Locate platelets.
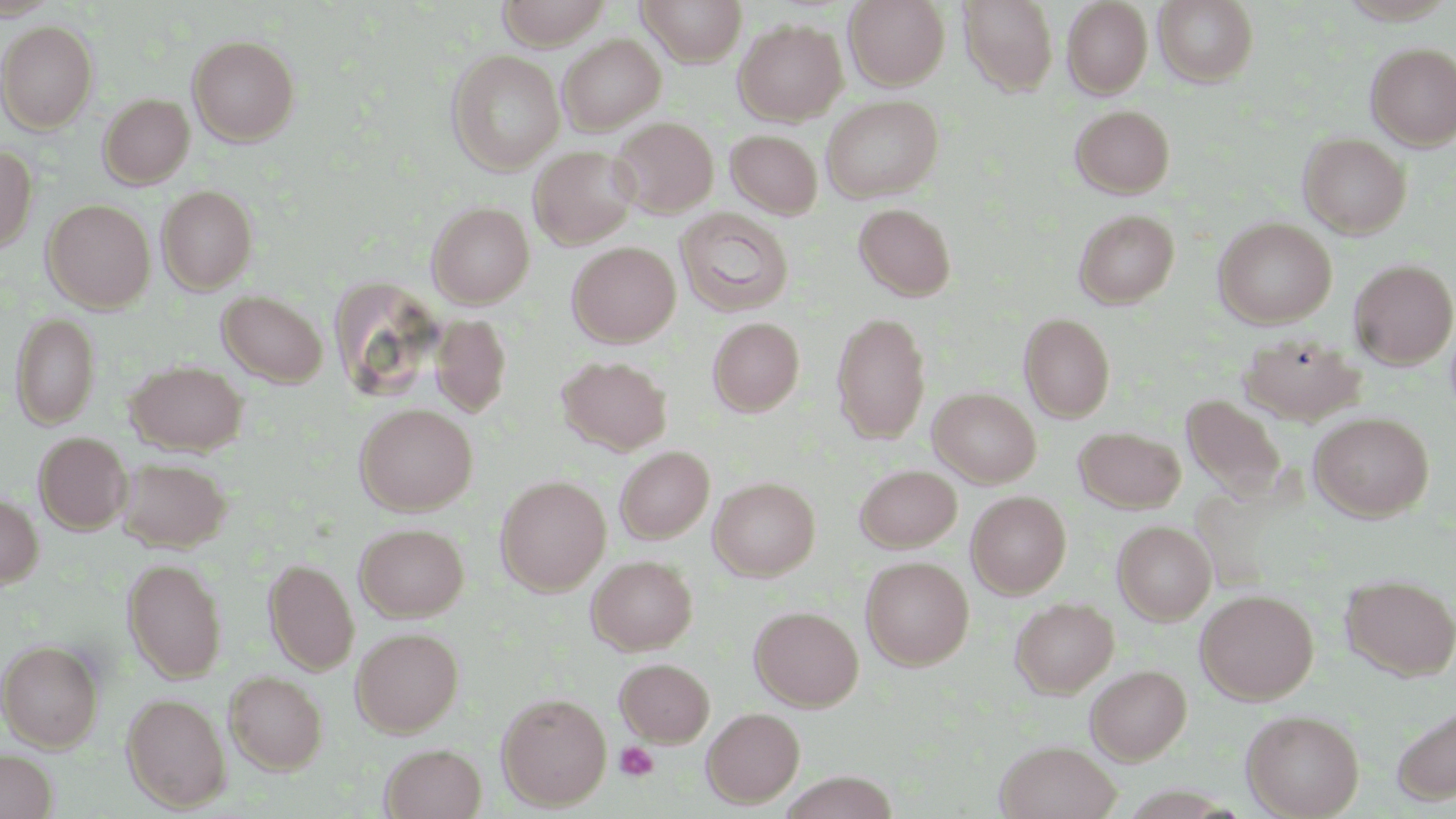

Approximate bounding boxes as (x1, y1, x2, y2) in pixels.
Platelets: (614, 740, 659, 782).

Uninfected red blood cell locations: (0, 0, 60, 19), (496, 0, 612, 48), (638, 0, 747, 66), (844, 0, 950, 89), (959, 0, 1059, 94), (1153, 0, 1258, 86), (1062, 1, 1153, 98), (733, 19, 847, 125), (0, 20, 99, 132), (188, 34, 300, 145), (558, 34, 665, 135), (1366, 42, 1456, 150), (446, 49, 565, 173), (99, 93, 194, 189), (822, 95, 943, 202), (1071, 105, 1175, 198), (610, 117, 719, 217), (726, 129, 822, 219), (1298, 132, 1411, 238), (0, 144, 37, 254), (528, 146, 640, 249), (157, 185, 258, 293), (43, 199, 155, 312), (427, 202, 534, 307), (854, 202, 958, 301), (675, 207, 795, 318), (1073, 208, 1180, 309), (1213, 218, 1336, 328), (568, 242, 680, 347), (1350, 259, 1455, 369), (217, 290, 328, 387), (831, 311, 931, 443), (11, 312, 100, 429), (1019, 312, 1116, 422), (430, 313, 512, 416), (707, 317, 805, 417), (1238, 332, 1365, 425), (557, 355, 672, 455), (126, 360, 247, 455), (928, 388, 1041, 488), (1181, 394, 1287, 502), (354, 402, 477, 515), (1309, 412, 1434, 521), (1074, 427, 1186, 513), (34, 431, 132, 534), (615, 446, 714, 543), (116, 456, 231, 553), (855, 465, 962, 552), (495, 475, 611, 594), (709, 477, 820, 580), (967, 491, 1071, 598), (0, 493, 43, 588), (1113, 521, 1216, 624), (355, 522, 469, 622), (587, 554, 697, 655), (860, 556, 974, 670), (263, 558, 358, 675), (123, 559, 227, 683), (1340, 574, 1456, 680), (1195, 590, 1318, 704), (1010, 597, 1119, 697), (749, 605, 864, 710), (351, 626, 464, 736), (0, 639, 104, 751), (614, 657, 715, 746), (1086, 664, 1191, 764), (225, 671, 328, 774), (122, 692, 231, 812), (497, 692, 611, 810), (1392, 703, 1456, 805), (702, 707, 805, 807), (1241, 709, 1365, 818), (995, 739, 1122, 819), (380, 743, 487, 819), (0, 749, 58, 819), (780, 772, 900, 819). Slide-level diagnosis: negative for blood parasites. One field of a larger specimen. Thin blood film. Image is 1456×819 pixels. May-Grünwald-Giemsa stain. Optical microscopy. 1000x magnification.